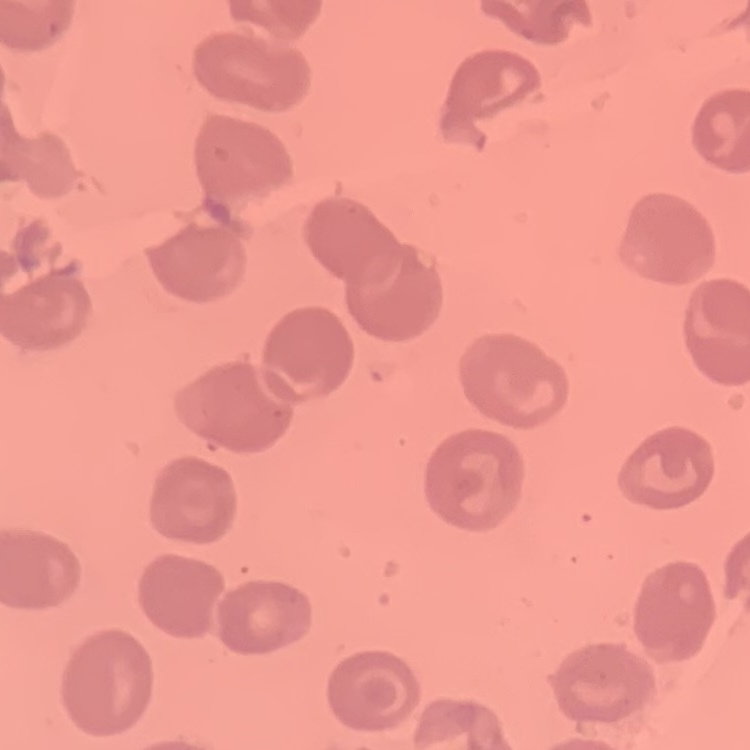

red blood cell morphology = no rouleaux formation
image type = square crop of a larger photomicrograph
stain = Field's or Giemsa
preparation = thin blood film